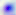

Micrograph. Toxoplasma gondii is seen. Captured at 400x magnification.